Give the extent of all Plasmodium vivax-infected red blood cells.
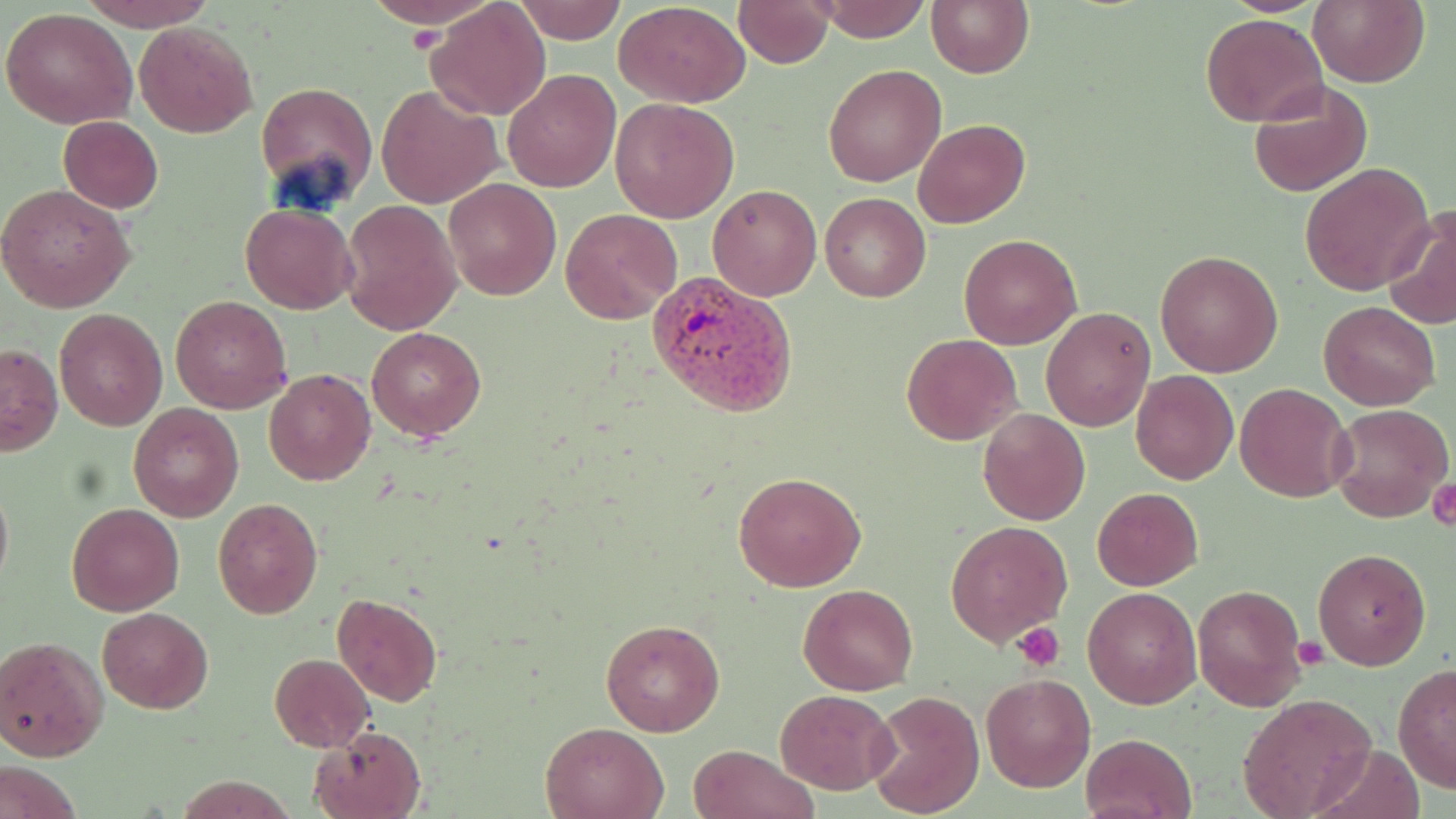
Approximate bounding boxes as named x1/y1/x2/y2 corners in pixels.
Plasmodium vivax-infected red blood cells: (x1=647, y1=275, x2=799, y2=420).

Uninfected red blood cell locations: (x1=79, y1=0, x2=220, y2=30), (x1=370, y1=0, x2=490, y2=32), (x1=734, y1=0, x2=836, y2=68), (x1=816, y1=0, x2=930, y2=43), (x1=926, y1=0, x2=1033, y2=78), (x1=1207, y1=0, x2=1337, y2=16), (x1=1306, y1=0, x2=1428, y2=87), (x1=512, y1=1, x2=626, y2=45), (x1=427, y1=2, x2=550, y2=122), (x1=614, y1=2, x2=751, y2=107), (x1=1, y1=7, x2=138, y2=129), (x1=1200, y1=13, x2=1329, y2=126), (x1=133, y1=22, x2=257, y2=138), (x1=823, y1=63, x2=947, y2=187), (x1=502, y1=67, x2=620, y2=192), (x1=1249, y1=79, x2=1372, y2=198), (x1=255, y1=80, x2=377, y2=207), (x1=502, y1=82, x2=730, y2=201), (x1=377, y1=83, x2=503, y2=210), (x1=611, y1=97, x2=739, y2=223), (x1=59, y1=116, x2=164, y2=213), (x1=914, y1=118, x2=1030, y2=229), (x1=1300, y1=163, x2=1435, y2=295), (x1=443, y1=178, x2=560, y2=299), (x1=708, y1=183, x2=822, y2=301), (x1=0, y1=185, x2=136, y2=313), (x1=820, y1=193, x2=930, y2=302), (x1=341, y1=201, x2=460, y2=335), (x1=240, y1=203, x2=358, y2=314), (x1=1383, y1=207, x2=1456, y2=331), (x1=559, y1=208, x2=682, y2=324), (x1=959, y1=235, x2=1082, y2=349), (x1=1155, y1=248, x2=1284, y2=377), (x1=169, y1=295, x2=291, y2=412), (x1=1317, y1=301, x2=1440, y2=410), (x1=1041, y1=307, x2=1155, y2=430), (x1=53, y1=308, x2=167, y2=431), (x1=366, y1=326, x2=487, y2=441), (x1=902, y1=333, x2=1022, y2=446), (x1=1, y1=342, x2=63, y2=456), (x1=263, y1=368, x2=376, y2=485), (x1=1130, y1=369, x2=1238, y2=485), (x1=1235, y1=382, x2=1353, y2=502), (x1=1329, y1=402, x2=1454, y2=524), (x1=129, y1=404, x2=245, y2=521), (x1=978, y1=408, x2=1091, y2=525), (x1=732, y1=471, x2=866, y2=592), (x1=0, y1=477, x2=13, y2=596), (x1=1092, y1=487, x2=1203, y2=590), (x1=212, y1=498, x2=324, y2=620), (x1=66, y1=501, x2=185, y2=616), (x1=944, y1=520, x2=1073, y2=644), (x1=1312, y1=546, x2=1432, y2=671), (x1=1192, y1=582, x2=1307, y2=712), (x1=799, y1=584, x2=917, y2=694), (x1=1081, y1=586, x2=1202, y2=709), (x1=332, y1=592, x2=444, y2=708), (x1=97, y1=607, x2=213, y2=713), (x1=600, y1=619, x2=725, y2=735), (x1=0, y1=635, x2=108, y2=762), (x1=269, y1=654, x2=375, y2=752), (x1=1393, y1=665, x2=1456, y2=794), (x1=980, y1=674, x2=1096, y2=792), (x1=774, y1=688, x2=897, y2=793), (x1=866, y1=690, x2=986, y2=818), (x1=1237, y1=694, x2=1376, y2=817), (x1=540, y1=720, x2=668, y2=819), (x1=310, y1=726, x2=427, y2=819), (x1=1080, y1=731, x2=1199, y2=819), (x1=1312, y1=742, x2=1424, y2=819), (x1=687, y1=744, x2=818, y2=819), (x1=0, y1=758, x2=84, y2=819). Platelet locations: (x1=409, y1=18, x2=452, y2=54), (x1=1428, y1=475, x2=1455, y2=534), (x1=1013, y1=621, x2=1067, y2=670), (x1=1296, y1=637, x2=1329, y2=669). Slide-level diagnosis: Plasmodium vivax. Captured at 1000x magnification. Thin blood film. Optical microscopy. Single field of view. May-Grünwald-Giemsa stain. Image is 1456×819 pixels.